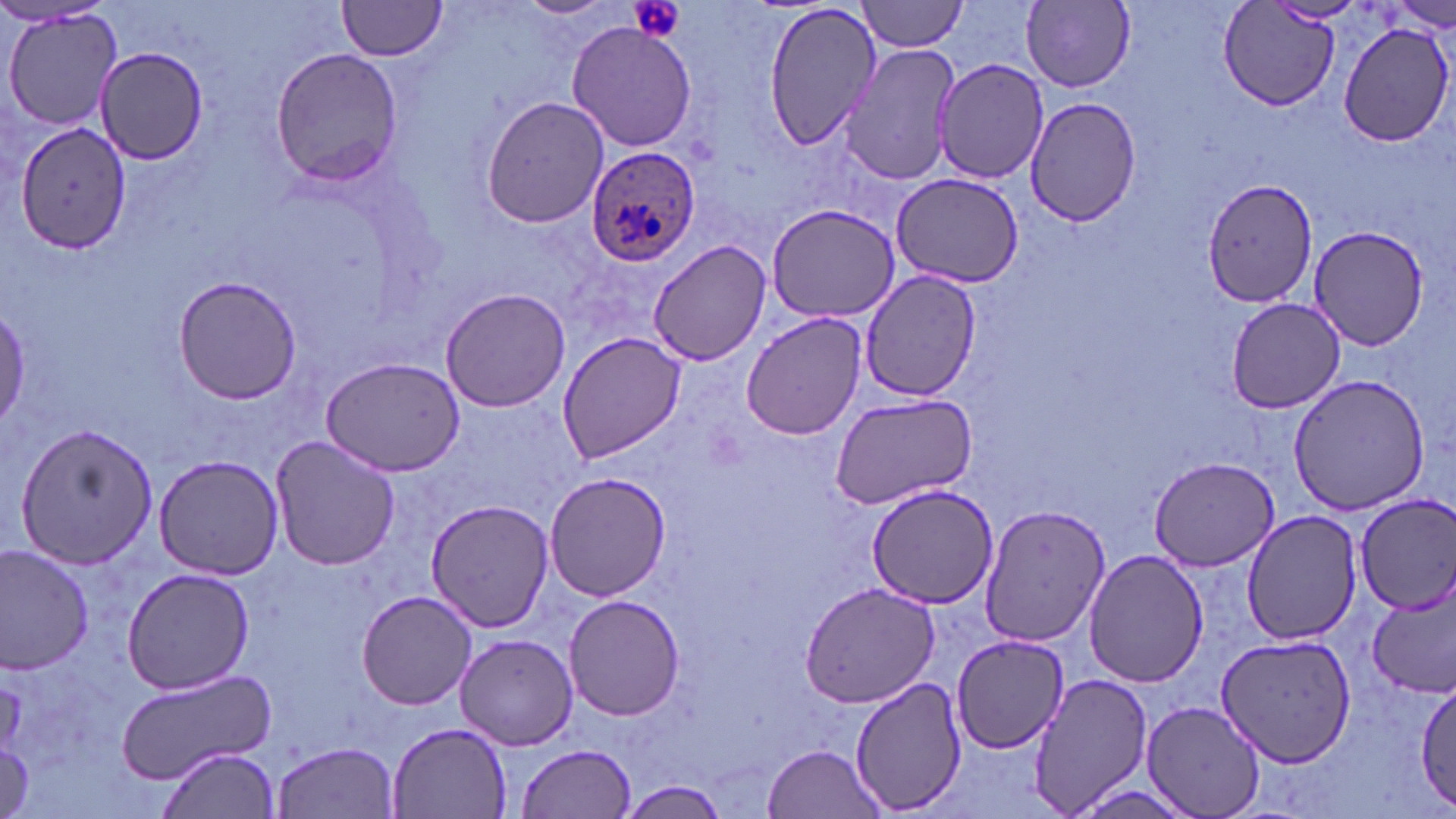
Summary:
  - Coordinate format: approximate bounding boxes as named x1/y1/x2/y2 corners in pixels
  - Platelet locations: (x1=629, y1=0, x2=686, y2=44)
  - Plasmodium ovale-infected red blood cell locations: (x1=585, y1=147, x2=699, y2=268)
  - Uninfected red blood cell locations: (x1=336, y1=0, x2=450, y2=61), (x1=515, y1=0, x2=620, y2=21), (x1=760, y1=0, x2=884, y2=155), (x1=858, y1=0, x2=972, y2=52), (x1=1021, y1=0, x2=1136, y2=90), (x1=1214, y1=1, x2=1343, y2=112), (x1=1385, y1=1, x2=1456, y2=32), (x1=2, y1=7, x2=123, y2=135), (x1=565, y1=20, x2=698, y2=154), (x1=1337, y1=22, x2=1455, y2=147), (x1=839, y1=44, x2=959, y2=187), (x1=92, y1=48, x2=209, y2=165), (x1=268, y1=48, x2=405, y2=186), (x1=935, y1=59, x2=1051, y2=185), (x1=481, y1=94, x2=611, y2=228), (x1=1026, y1=97, x2=1140, y2=227), (x1=12, y1=120, x2=134, y2=254), (x1=890, y1=173, x2=1026, y2=287), (x1=1202, y1=178, x2=1318, y2=308), (x1=764, y1=202, x2=902, y2=321), (x1=1307, y1=227, x2=1432, y2=353), (x1=649, y1=240, x2=771, y2=366), (x1=860, y1=270, x2=981, y2=403), (x1=172, y1=276, x2=301, y2=405), (x1=439, y1=286, x2=571, y2=413), (x1=1225, y1=298, x2=1346, y2=414), (x1=741, y1=311, x2=867, y2=442), (x1=557, y1=332, x2=687, y2=463), (x1=319, y1=358, x2=465, y2=477), (x1=1285, y1=372, x2=1432, y2=514), (x1=828, y1=392, x2=979, y2=510), (x1=13, y1=420, x2=160, y2=568), (x1=269, y1=436, x2=403, y2=573), (x1=153, y1=453, x2=286, y2=578), (x1=1150, y1=456, x2=1280, y2=570), (x1=543, y1=470, x2=671, y2=602), (x1=869, y1=486, x2=996, y2=610), (x1=1353, y1=493, x2=1456, y2=615), (x1=424, y1=498, x2=554, y2=632), (x1=981, y1=501, x2=1113, y2=649), (x1=1242, y1=511, x2=1364, y2=645), (x1=0, y1=546, x2=96, y2=674), (x1=1083, y1=549, x2=1209, y2=688), (x1=122, y1=566, x2=256, y2=694), (x1=798, y1=580, x2=943, y2=708), (x1=1368, y1=583, x2=1456, y2=698), (x1=355, y1=589, x2=479, y2=711), (x1=564, y1=594, x2=686, y2=722), (x1=1212, y1=631, x2=1357, y2=768), (x1=455, y1=632, x2=579, y2=750), (x1=953, y1=634, x2=1071, y2=754), (x1=116, y1=666, x2=275, y2=782), (x1=1028, y1=672, x2=1152, y2=814), (x1=849, y1=674, x2=965, y2=813), (x1=1413, y1=682, x2=1455, y2=810), (x1=1142, y1=702, x2=1264, y2=819), (x1=386, y1=722, x2=514, y2=816), (x1=274, y1=742, x2=399, y2=817), (x1=520, y1=743, x2=637, y2=818), (x1=759, y1=743, x2=888, y2=819), (x1=158, y1=748, x2=280, y2=819), (x1=615, y1=780, x2=732, y2=816)
  - Slide-level diagnosis: Plasmodium ovale
  - Preparation: thin blood film
  - Image size: 1456×819 pixels
  - Stain: May-Grünwald-Giemsa
  - Modality: light microscopy
  - Field of view: one of a larger specimen
  - Magnification: 1000x